Evaluate for parasitized red blood cells.
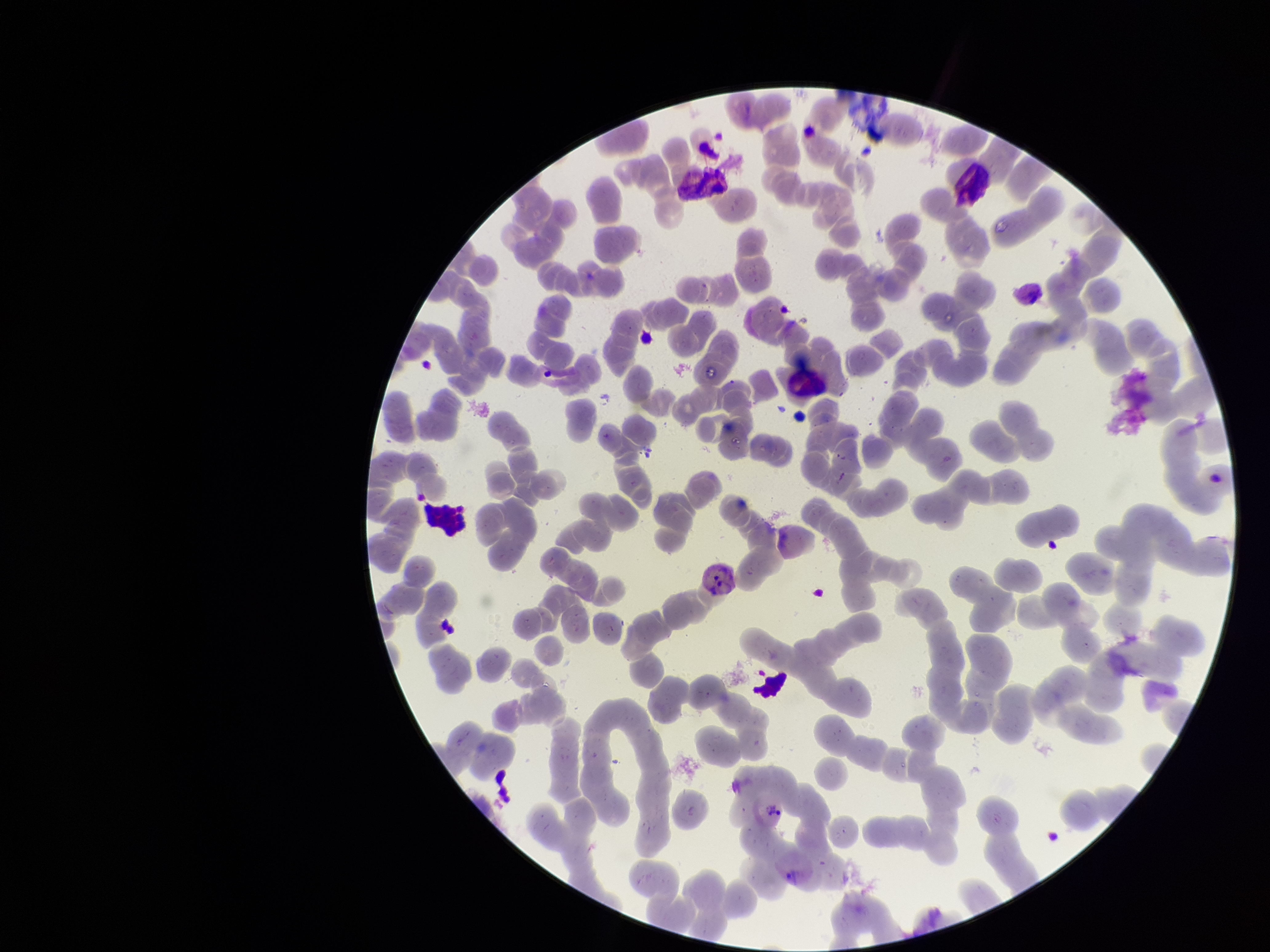

Seen.

Summary:
  - Preparation: thin blood smear
  - Patient malaria status: positive
  - Capture: smartphone photograph through the microscope eyepiece
  - Red blood cell count: 231
  - Species reported for this patient: Plasmodium vivax
  - Parasitized red blood cell count: 1
  - Field of view: one from this slide
  - Image size: 1270×952 pixels
  - Stain: Giemsa